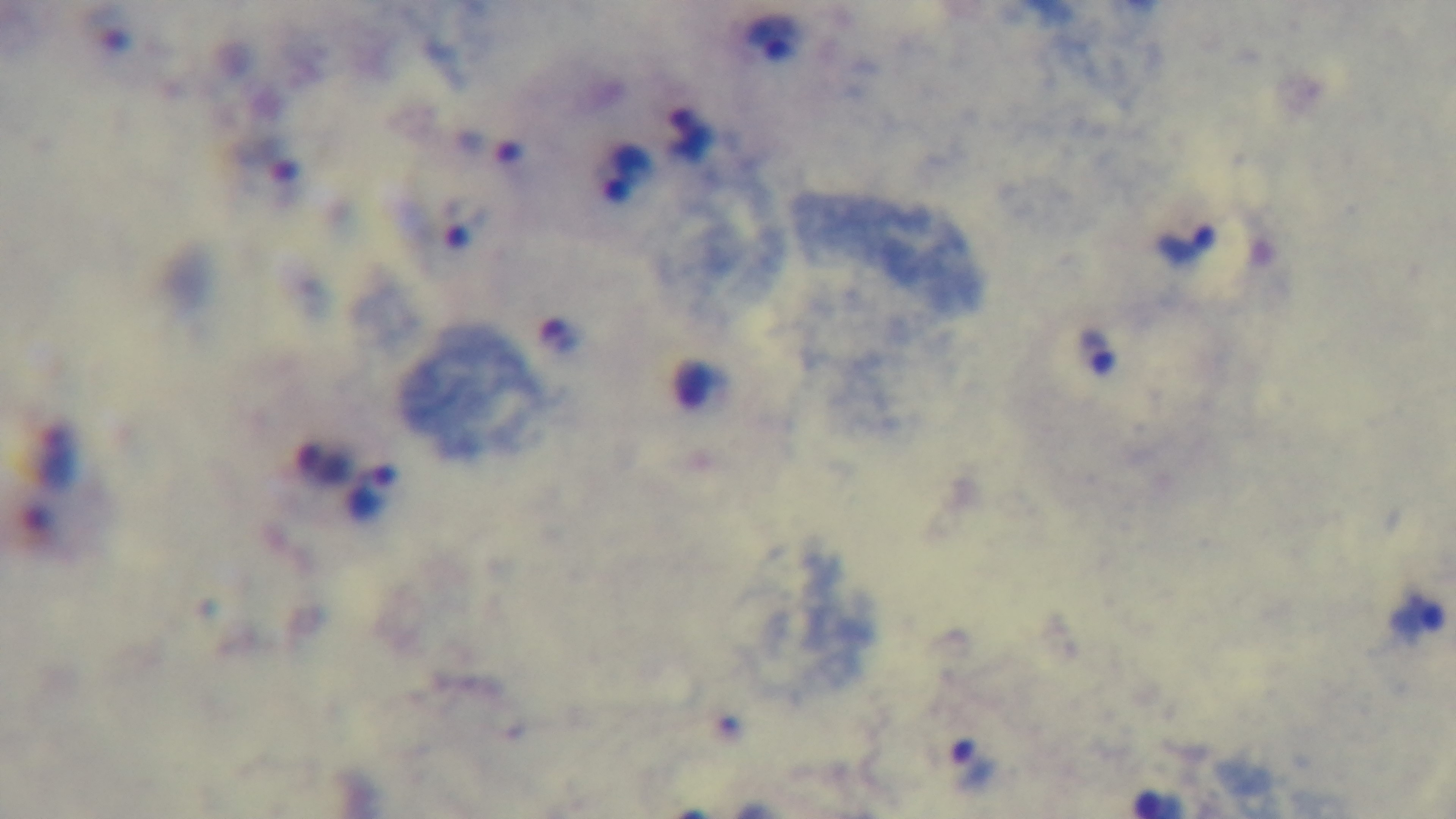

field of view = one from the slide
capture = mounted 4K digital camera
stain = Giemsa
malaria status = infected
objective = 100x oil immersion
modality = light microscopy
preparation = thick